Classify this cell by malaria status.
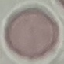
Uninfected.

Summary:
  - Capture: smartphone camera at the microscope eyepiece
  - Stain: Giemsa
  - Image type: cell patch, automatically extracted from a larger field of view and resized to 64 × 64 pixels
  - Preparation: thin blood film